Locate every parasitized RBC.
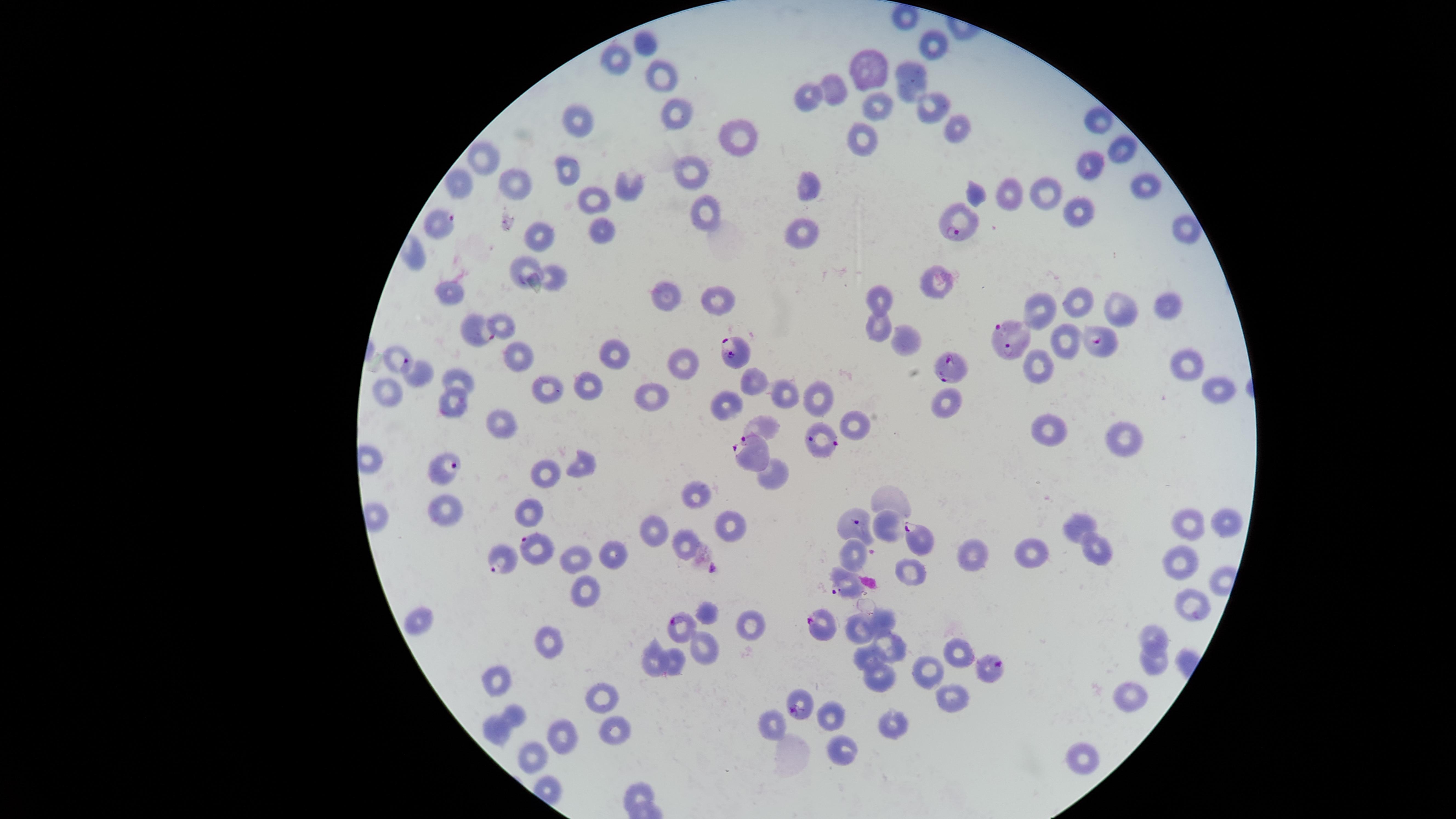

Approximate marker points as {x, y} in pixels.
Parasitized RBCs: {439, 222}, {959, 226}, {470, 329}, {1012, 336}, {1094, 340}, {736, 348}, {952, 369}, {418, 372}, {826, 437}, {755, 451}, {450, 464}, {851, 526}, {918, 540}, {536, 543}, {501, 557}, {846, 583}, {683, 624}, {823, 624}, {990, 668}, {796, 699}.

field of view = single
preparation = thin blood film
species = Plasmodium falciparum
uninfected RBCs = approximate marker points as {x, y} in pixels: {644, 45}, {935, 46}, {616, 61}, {869, 65}, {913, 77}, {661, 78}, {835, 88}, {810, 95}, {932, 100}, {875, 103}, {675, 113}, {1101, 120}, {577, 122}, {956, 124}, {742, 136}, {864, 138}, {1118, 145}, {485, 157}, {1086, 164}, {567, 169}, {691, 172}, {462, 182}, {510, 182}, {810, 182}, {1144, 184}, {630, 186}, {1007, 194}, {591, 199}, {1075, 210}, {705, 213}, {803, 228}, {1181, 228}, {600, 233}, {536, 236}, {525, 272}, {938, 278}, {556, 280}, {449, 292}, {664, 297}, {716, 300}, {881, 300}, {1078, 301}, {1164, 303}, {1043, 305}, {1120, 305}, {504, 324}, {878, 324}, {906, 340}, {1062, 340}, {397, 354}, {611, 354}, {516, 355}, {687, 361}, {1183, 364}, {1034, 365}, {459, 378}, {749, 382}, {1216, 385}, {543, 387}, {585, 388}, {782, 390}, {390, 394}, {818, 395}, {649, 399}, {939, 402}, {725, 404}, {451, 407}, {501, 422}, {858, 422}, {1045, 425}, {764, 429}, {1125, 436}, {584, 461}, {544, 472}, {773, 475}, {697, 494}, {895, 497}, {444, 508}, {528, 514}, {728, 524}, {1081, 524}, {1225, 524}, {1190, 526}, {654, 528}, {885, 528}, {682, 544}, {611, 549}, {852, 552}, {1094, 554}, {978, 555}, {575, 557}, {1027, 557}, {1179, 563}, {915, 572}, {580, 586}, {706, 608}, {1190, 608}, {417, 618}, {752, 621}, {880, 622}, {856, 631}, {1151, 638}, {547, 641}, {703, 649}, {892, 651}, {958, 652}, {863, 658}, {672, 660}, {657, 661}, {1153, 661}, {929, 669}, {882, 676}, {500, 680}, {604, 697}, {1131, 697}, {952, 699}, {832, 712}, {516, 713}, {774, 721}, {891, 723}, {495, 729}, {611, 730}, {559, 737}, {841, 749}, {533, 753}, {1082, 761}, {638, 790}
visible region = circular
image size = 1456×819 pixels
stain = Giemsa
capture = smartphone photograph through the microscope eyepiece